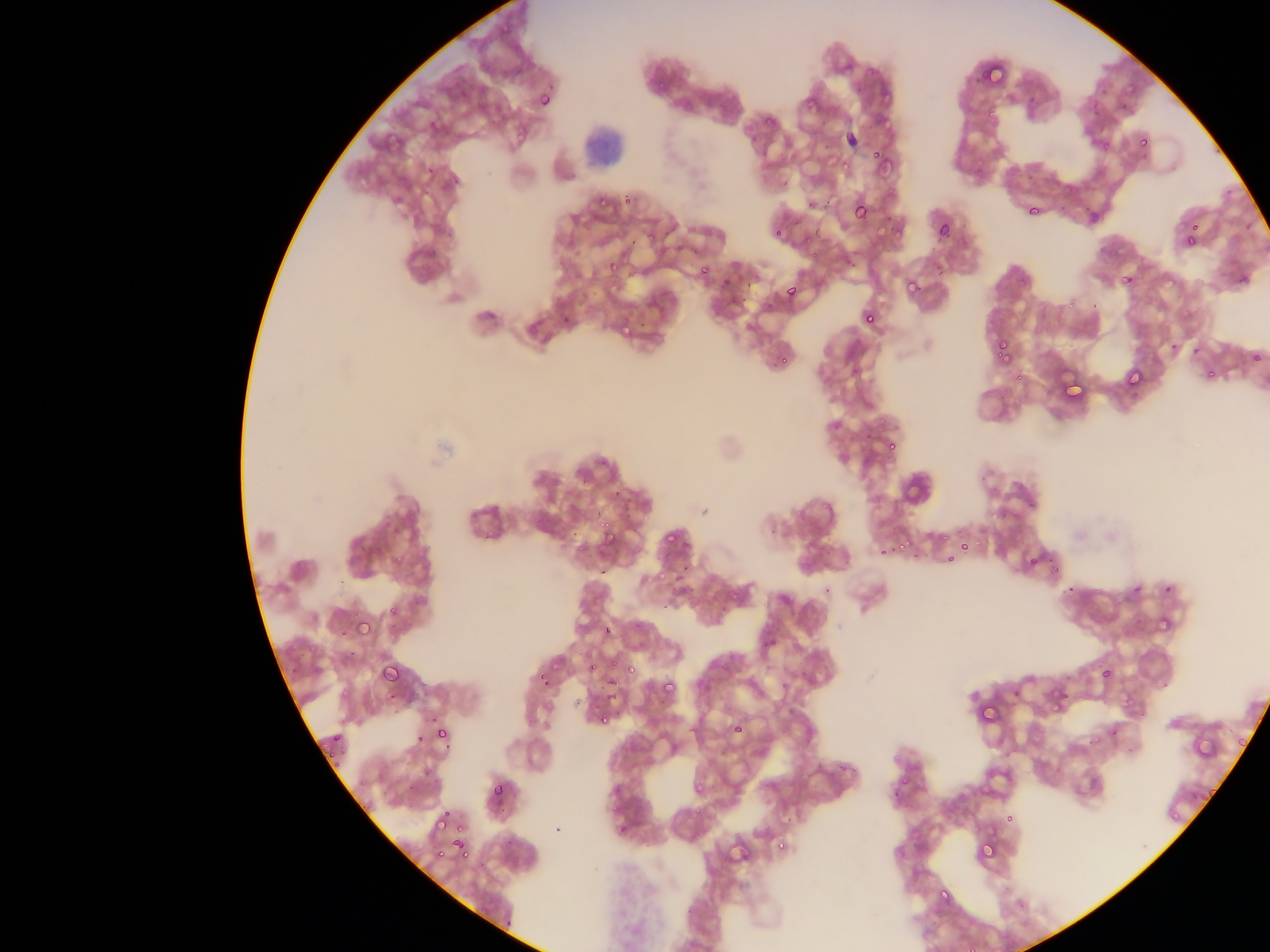

Approximate bounding boxes as {left, top, right, bottom} in pixels.
Summary:
  - Plasmodium parasite locations: {492, 14, 526, 35}, {835, 63, 852, 75}, {981, 64, 1010, 85}, {643, 78, 664, 91}, {1097, 78, 1109, 100}, {536, 87, 559, 113}, {801, 88, 818, 107}, {1120, 99, 1130, 110}, {843, 111, 862, 152}, {763, 112, 781, 128}, {425, 113, 448, 134}, {1134, 117, 1156, 147}, {517, 122, 534, 146}, {742, 132, 754, 147}, {392, 133, 402, 145}, {1094, 134, 1115, 156}, {833, 141, 855, 167}, {868, 145, 895, 176}, {426, 161, 439, 182}, {803, 193, 816, 216}, {591, 194, 605, 208}, {622, 196, 636, 214}, {850, 199, 872, 225}, {1025, 203, 1042, 220}, {1186, 209, 1197, 231}, {772, 216, 794, 246}, {934, 220, 954, 243}, {809, 223, 823, 237}, {1182, 231, 1200, 252}, {628, 233, 650, 255}, {803, 234, 813, 249}, {602, 258, 621, 278}, {697, 265, 714, 285}, {1119, 271, 1138, 291}, {720, 274, 734, 291}, {901, 275, 926, 303}, {783, 282, 802, 304}, {559, 301, 581, 328}, {618, 305, 637, 334}, {859, 307, 880, 330}, {1165, 324, 1189, 358}, {994, 340, 1014, 364}, {1183, 344, 1198, 361}, {1246, 353, 1264, 364}, {1123, 365, 1147, 392}, {1196, 365, 1214, 380}, {877, 431, 905, 463}, {883, 437, 901, 459}, {478, 511, 510, 546}, {596, 519, 620, 548}, {662, 519, 680, 546}, {955, 539, 975, 561}, {894, 540, 904, 553}, {874, 549, 884, 560}, {940, 552, 950, 572}, {1025, 552, 1043, 572}, {667, 563, 683, 585}, {1155, 584, 1172, 598}, {385, 601, 403, 621}, {1150, 604, 1181, 636}, {354, 617, 375, 640}, {601, 622, 617, 640}, {377, 656, 406, 687}, {587, 656, 604, 674}, {625, 661, 639, 675}, {536, 663, 552, 693}, {1099, 663, 1116, 685}, {602, 672, 620, 698}, {658, 678, 679, 702}, {1048, 686, 1075, 716}, {974, 699, 1000, 733}, {594, 709, 614, 729}, {729, 720, 749, 741}, {433, 725, 452, 747}, {327, 728, 343, 740}, {412, 728, 424, 750}, {1233, 732, 1248, 746}, {323, 746, 341, 760}, {424, 760, 440, 773}, {690, 764, 708, 795}, {489, 780, 511, 805}, {1206, 786, 1224, 809}, {1162, 806, 1179, 824}, {430, 811, 450, 831}, {1002, 811, 1016, 829}, {454, 831, 472, 860}, {425, 832, 454, 862}, {976, 833, 1001, 864}, {777, 834, 795, 856}, {936, 890, 951, 902}, {962, 941, 974, 952}
  - Field of view: single
  - Country: Ghana
  - Capture: mobile-phone photograph through a microscope
  - Preparation: thin blood smear
  - Image size: 1270×952 pixels